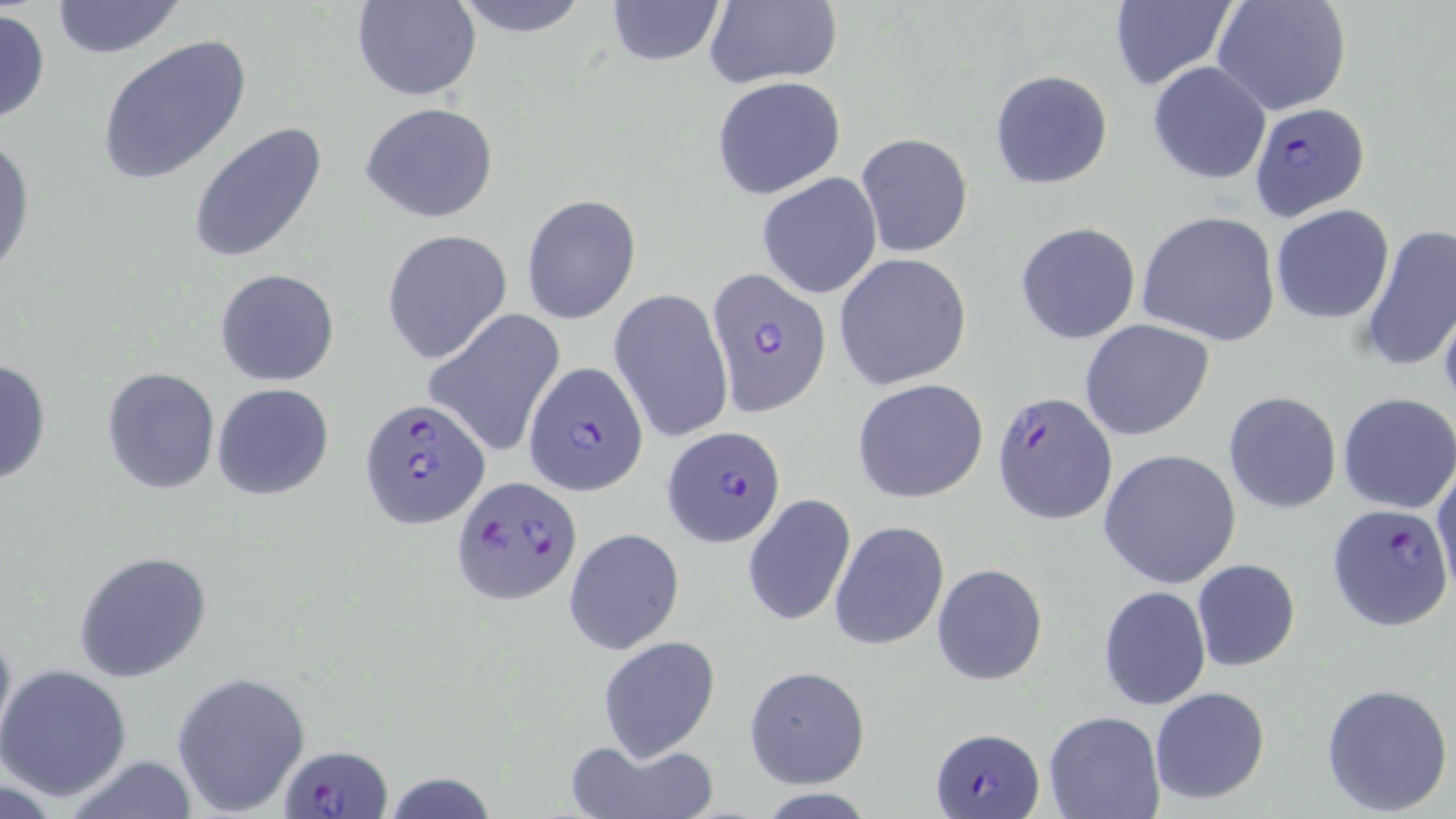

slide-level diagnosis = Plasmodium falciparum
stain = May-Grünwald-Giemsa
modality = optical microscopy
magnification = 1000x
image size = 1456×819 pixels
Plasmodium falciparum-infected red blood cell locations (subset) = approximate bounding boxes as [x1, y1, x2, y2] in pixels: [1249, 103, 1370, 219], [707, 268, 832, 417], [526, 360, 652, 497], [992, 389, 1117, 526], [359, 398, 491, 530], [662, 426, 785, 548], [451, 475, 582, 606], [932, 726, 1046, 817], [282, 743, 393, 819]
preparation = thin blood smear
field of view = one of a larger specimen
uninfected red blood cell locations (subset) = approximate bounding boxes as [x1, y1, x2, y2] in pixels: [49, 0, 186, 59], [447, 0, 595, 37], [603, 0, 726, 66], [704, 0, 843, 89], [1108, 0, 1235, 92], [1212, 0, 1352, 117], [353, 1, 479, 100], [0, 8, 50, 126], [96, 35, 252, 186], [1146, 61, 1271, 186], [989, 68, 1115, 191], [711, 76, 845, 199], [360, 102, 498, 223], [188, 122, 330, 262], [0, 128, 35, 280], [856, 132, 973, 257], [758, 173, 883, 299], [520, 192, 641, 325], [1270, 204, 1395, 324], [1137, 211, 1282, 346], [1014, 221, 1142, 345], [1359, 222, 1456, 374], [381, 229, 512, 365], [834, 253, 972, 390], [214, 268, 341, 387], [612, 287, 732, 446], [1437, 293, 1456, 418], [423, 310, 566, 456], [1081, 319, 1214, 439], [0, 356, 52, 487], [101, 366, 221, 495], [852, 378, 989, 503], [211, 383, 335, 499], [1224, 391, 1341, 513], [1336, 393, 1455, 514], [1098, 448, 1243, 589], [1432, 464, 1455, 598], [741, 494, 855, 628], [829, 520, 949, 650], [564, 528, 684, 654], [74, 551, 213, 685], [1192, 558, 1301, 672], [932, 564, 1049, 685], [1098, 584, 1212, 711], [0, 617, 17, 752], [597, 635, 721, 761], [0, 664, 132, 801], [744, 665, 870, 788], [171, 671, 312, 817], [1320, 681, 1454, 816], [1149, 687, 1271, 808], [1043, 709, 1164, 819], [565, 735, 719, 819], [60, 756, 195, 818]